Locate every blood parasite and identify its species.
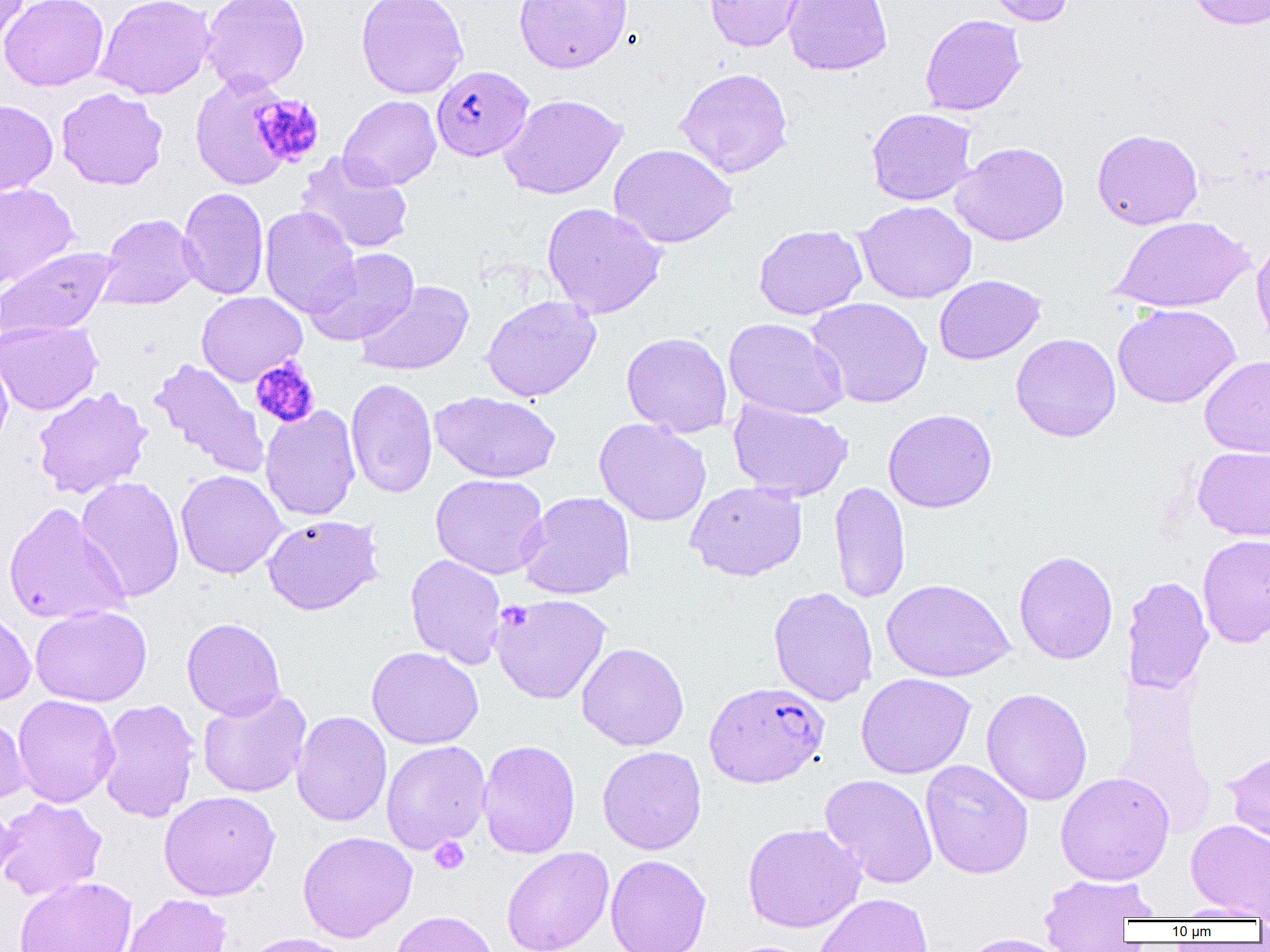

Approximate bounding boxes as (x1,y1)-(x2,y2) corner pairs in pixels.
Plasmodium falciparum-infected red blood cells: (431,65)-(534,161), (704,681)-(829,788).
No Plasmodium ovale, Plasmodium malariae, Plasmodium vivax, Babesia divergens, or Trypanosoma brucei observed.

Summary:
  - Uninfected red blood cell locations: (0,0)-(30,49), (1,0)-(109,91), (95,0)-(216,100), (201,0)-(310,93), (356,0)-(469,99), (513,0)-(633,73), (704,0)-(807,52), (782,0)-(893,76), (981,0)-(1076,26), (1186,0)-(1270,30), (919,14)-(1026,116), (675,67)-(794,178), (190,71)-(299,190), (56,87)-(168,190), (498,94)-(628,200), (338,95)-(441,190), (0,100)-(58,195), (866,108)-(977,206), (1091,128)-(1204,230), (950,142)-(1070,246), (608,143)-(738,249), (295,153)-(414,254), (0,182)-(79,291), (178,187)-(269,300), (855,200)-(977,304), (542,202)-(667,319), (260,206)-(360,318), (98,213)-(200,311), (1112,215)-(1255,313), (753,224)-(867,320), (1252,236)-(1270,353), (0,246)-(120,339), (303,248)-(420,346), (933,274)-(1046,365), (354,281)-(474,377), (196,291)-(307,386), (481,295)-(601,402), (806,297)-(933,409), (1113,303)-(1240,409), (723,317)-(848,420), (0,320)-(102,416), (621,332)-(733,438), (1011,333)-(1121,442), (0,347)-(13,453), (1199,356)-(1270,458), (149,358)-(269,479), (345,378)-(437,498), (33,387)-(152,498), (429,391)-(561,483), (728,399)-(853,501), (260,404)-(361,521), (883,408)-(997,513), (594,418)-(712,526), (1192,446)-(1270,541), (175,470)-(287,579), (430,473)-(549,579), (75,476)-(185,603), (685,480)-(807,581), (829,481)-(911,604), (517,491)-(635,600), (2,502)-(129,626), (262,514)-(384,615), (1197,534)-(1270,649), (1014,550)-(1118,664), (405,553)-(506,669), (1122,576)-(1214,696), (882,578)-(1014,683), (768,586)-(878,707), (489,593)-(612,704), (30,605)-(152,707), (0,608)-(36,705), (182,618)-(286,721), (576,643)-(689,751), (367,646)-(484,749), (856,672)-(977,779), (981,688)-(1092,807), (197,689)-(312,799), (12,695)-(120,808), (97,698)-(201,822), (291,710)-(392,827), (0,712)-(31,806), (477,739)-(581,859), (381,740)-(490,853), (597,746)-(707,855), (1224,748)-(1270,854), (920,760)-(1034,879), (1055,771)-(1175,884), (819,774)-(938,889), (159,791)-(280,901), (0,797)-(107,900), (0,799)-(18,890), (1186,819)-(1270,920), (742,822)-(866,933), (297,831)-(417,942), (501,846)-(614,952), (605,854)-(711,952), (1038,873)-(1159,949), (15,876)-(137,952), (813,892)-(933,952), (120,893)-(232,952), (1168,902)-(1269,922), (390,910)-(499,952), (240,932)-(356,952), (956,933)-(1072,952)
  - Platelet locations: (251,94)-(325,167), (250,356)-(320,428), (504,603)-(531,633), (429,836)-(469,875)
  - Slide-level diagnosis: Plasmodium falciparum
  - Modality: optical microscopy
  - Magnification: 1000x
  - Image size: 1270×952 pixels
  - Preparation: thin blood film
  - Field of view: one of a larger specimen